State which parasite is depicted.
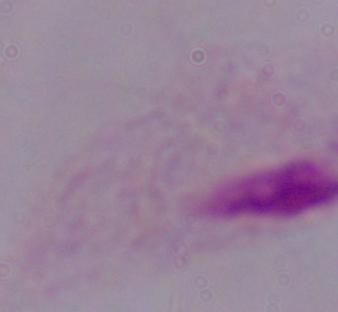

This is a trichomonad.

Summary:
  - Magnification: 1000x
  - Modality: micrograph